Describe the morphology of the erythrocytes.
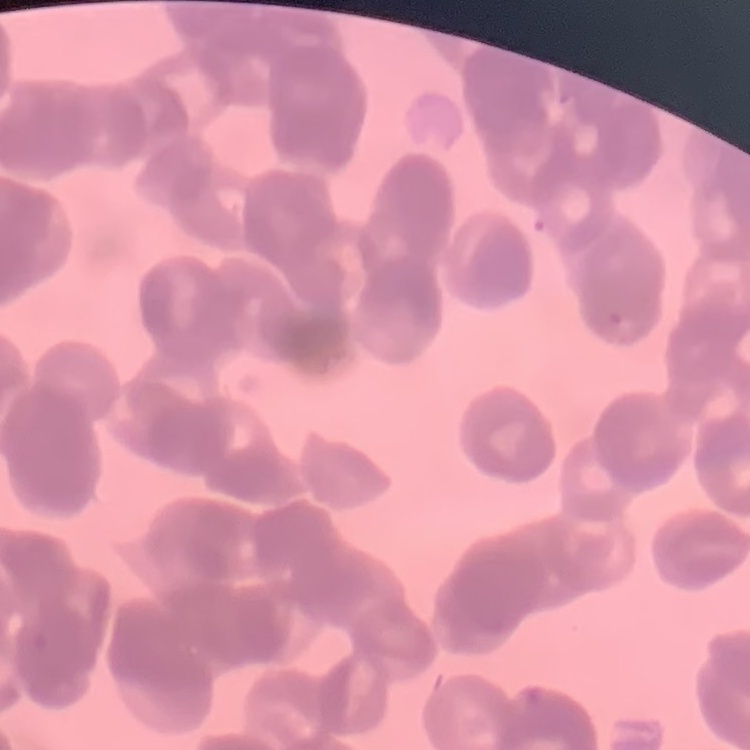
Rouleaux formation.

Square crop of a larger photomicrograph. Thin peripheral smear. Field's or Giemsa stain.